Report the malaria status of this cell.
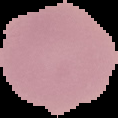

Uninfected.

Segmented cell region on a black background. Image is 118×118 pixels. From a thin blood film.